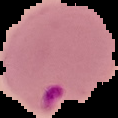

preparation = thin blood smear
malaria status = parasitized
image size = 118×118 pixels
image type = cell region segmented out of the field of view; surrounding area masked to black